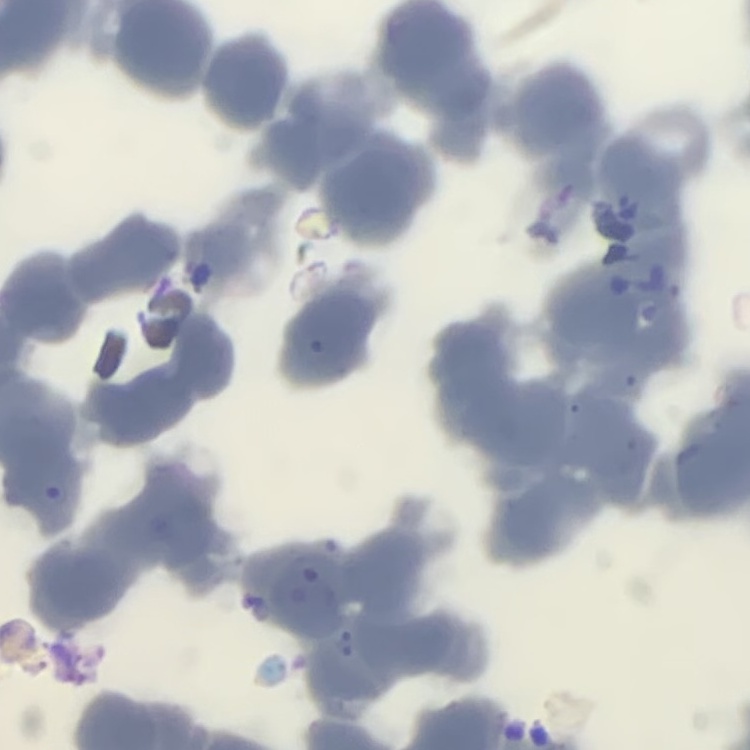

The red blood cells exhibit rouleaux formation. One tile cut from a larger photomicrograph. Stained with either Field's or Giemsa. Thin blood film.